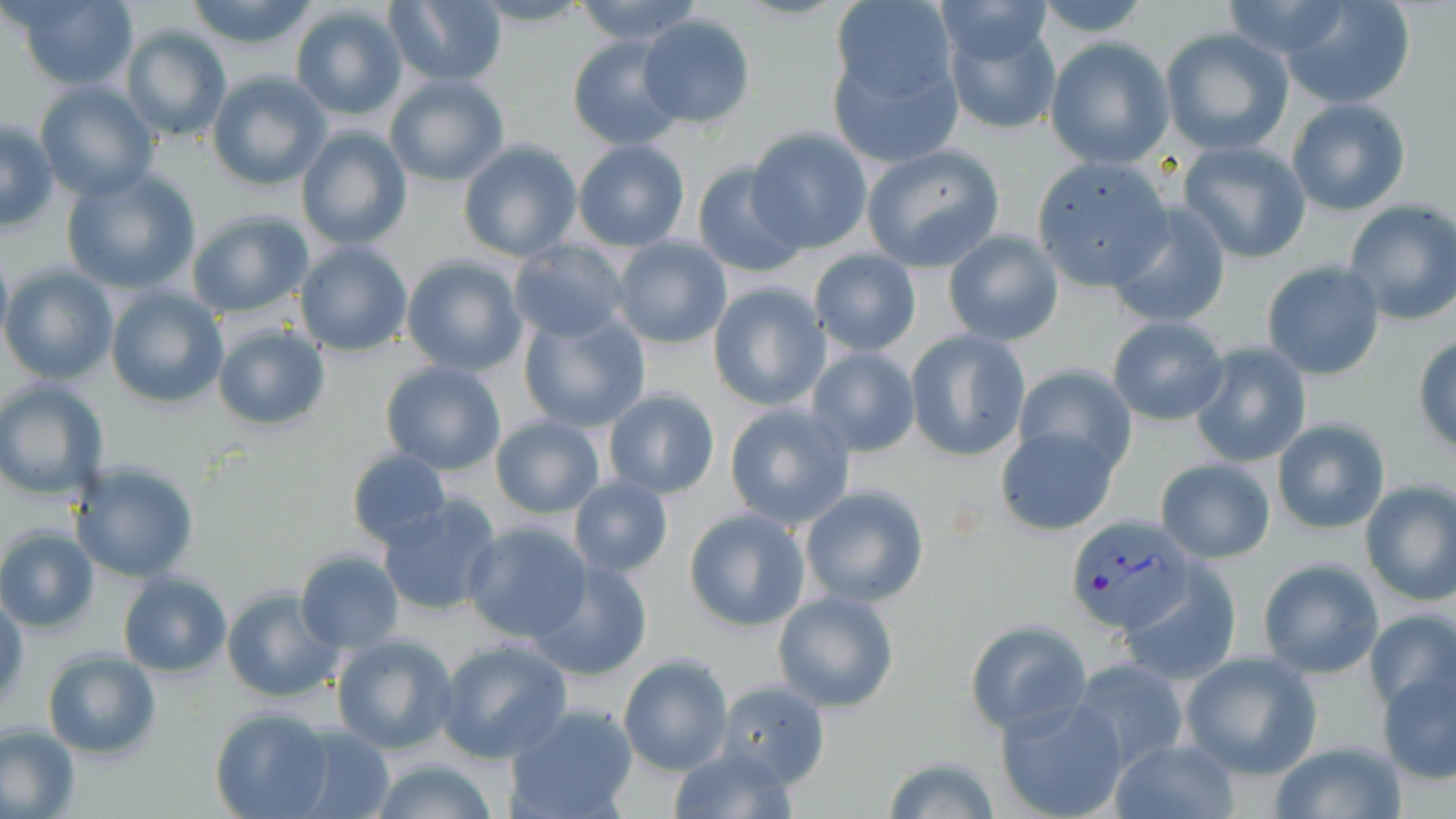
{
  "slide_level_diagnosis": "Plasmodium vivax",
  "modality": "optical microscopy",
  "preparation": "thin blood film",
  "plasmodium_vivax_infected_red_blood_cell_locations": "approximate bounding boxes as [x1, y1, x2, y2] in pixels: [1066, 516, 1197, 633]",
  "stain": "May-Grünwald-Giemsa",
  "field_of_view": "single",
  "uninfected_red_blood_cell_locations": "approximate bounding boxes as [x1, y1, x2, y2] in pixels: [14, 0, 139, 92], [184, 0, 319, 50], [468, 0, 595, 30], [571, 0, 706, 46], [929, 0, 1059, 66], [1032, 0, 1154, 38], [1220, 0, 1359, 60], [1276, 0, 1417, 109], [385, 1, 507, 86], [828, 1, 960, 128], [290, 4, 408, 121], [941, 12, 1063, 137], [638, 14, 756, 129], [120, 25, 233, 146], [1160, 27, 1294, 156], [567, 35, 686, 151], [1045, 38, 1174, 169], [208, 70, 330, 192], [384, 73, 509, 187], [33, 82, 161, 201], [1286, 97, 1412, 216], [1, 120, 57, 231], [296, 125, 414, 251], [747, 126, 873, 253], [458, 139, 581, 263], [572, 140, 690, 251], [1176, 140, 1313, 264], [862, 144, 1005, 270], [1030, 157, 1174, 290], [691, 161, 808, 279], [61, 167, 201, 295], [1342, 200, 1456, 325], [1105, 201, 1232, 329], [185, 211, 314, 318], [943, 229, 1064, 347], [612, 237, 732, 350], [508, 239, 630, 343], [294, 241, 413, 356], [0, 242, 12, 351], [808, 248, 922, 356], [400, 255, 526, 377], [1262, 260, 1385, 380], [0, 265, 118, 385], [707, 281, 831, 411], [108, 286, 228, 408], [517, 308, 650, 434], [1107, 316, 1230, 425], [213, 322, 330, 433], [906, 330, 1031, 462], [1412, 333, 1456, 455], [1189, 342, 1312, 468], [806, 345, 921, 457], [381, 361, 507, 476], [1010, 363, 1136, 479], [0, 380, 109, 500], [603, 388, 720, 500], [723, 403, 856, 531], [491, 417, 604, 518], [1272, 417, 1390, 535], [994, 425, 1118, 536], [347, 448, 451, 547], [1156, 456, 1276, 563], [68, 461, 199, 583], [568, 475, 673, 579], [1357, 480, 1456, 607], [799, 485, 930, 607], [376, 495, 503, 619], [683, 508, 808, 631], [463, 522, 595, 642], [0, 526, 99, 632], [295, 551, 404, 651], [525, 558, 654, 680], [1257, 558, 1383, 679], [1117, 565, 1242, 686], [118, 572, 231, 676], [221, 588, 343, 703], [772, 589, 899, 712], [0, 596, 28, 706], [1366, 609, 1455, 716], [965, 619, 1090, 735], [330, 634, 458, 755], [434, 639, 574, 764], [42, 650, 160, 758], [1179, 651, 1321, 779], [618, 653, 733, 777], [1067, 657, 1192, 774], [1376, 667, 1456, 783], [715, 680, 831, 787], [995, 694, 1129, 819], [503, 705, 640, 819], [210, 709, 332, 819], [0, 725, 80, 818], [287, 727, 395, 819], [1110, 739, 1239, 818], [1266, 740, 1406, 819], [666, 743, 800, 819], [882, 756, 1001, 818], [369, 759, 502, 819]",
  "magnification": "1000x",
  "image_size": "1456×819 pixels"
}